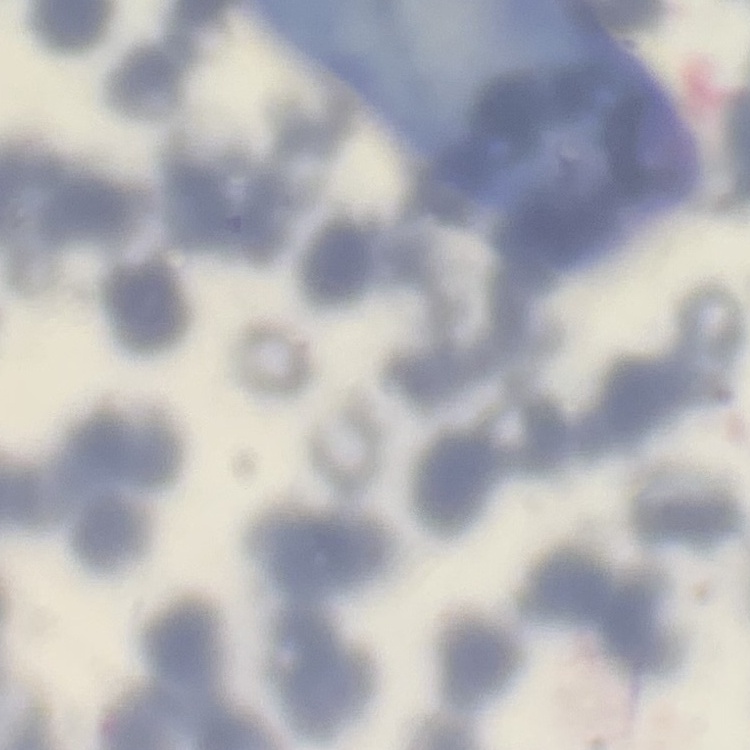
The red blood cells exhibit rouleaux formation. Stained with either Field's or Giemsa. One tile cut from a larger photomicrograph. Thin blood film.